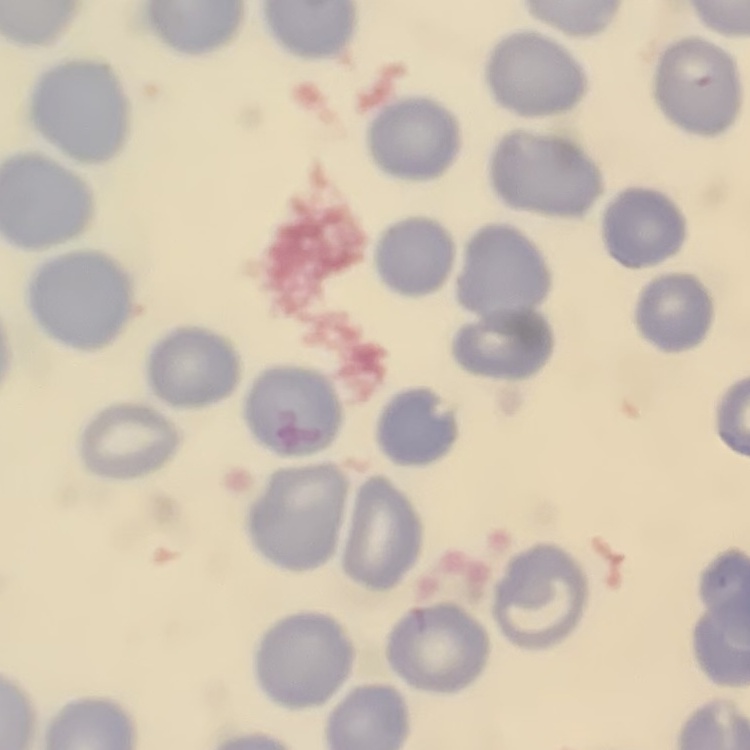
The erythrocytes exhibit no rouleaux formation. Field's or Giemsa stain. Thin blood smear. Square crop of a larger photomicrograph.